Point out each Plasmodium parasite.
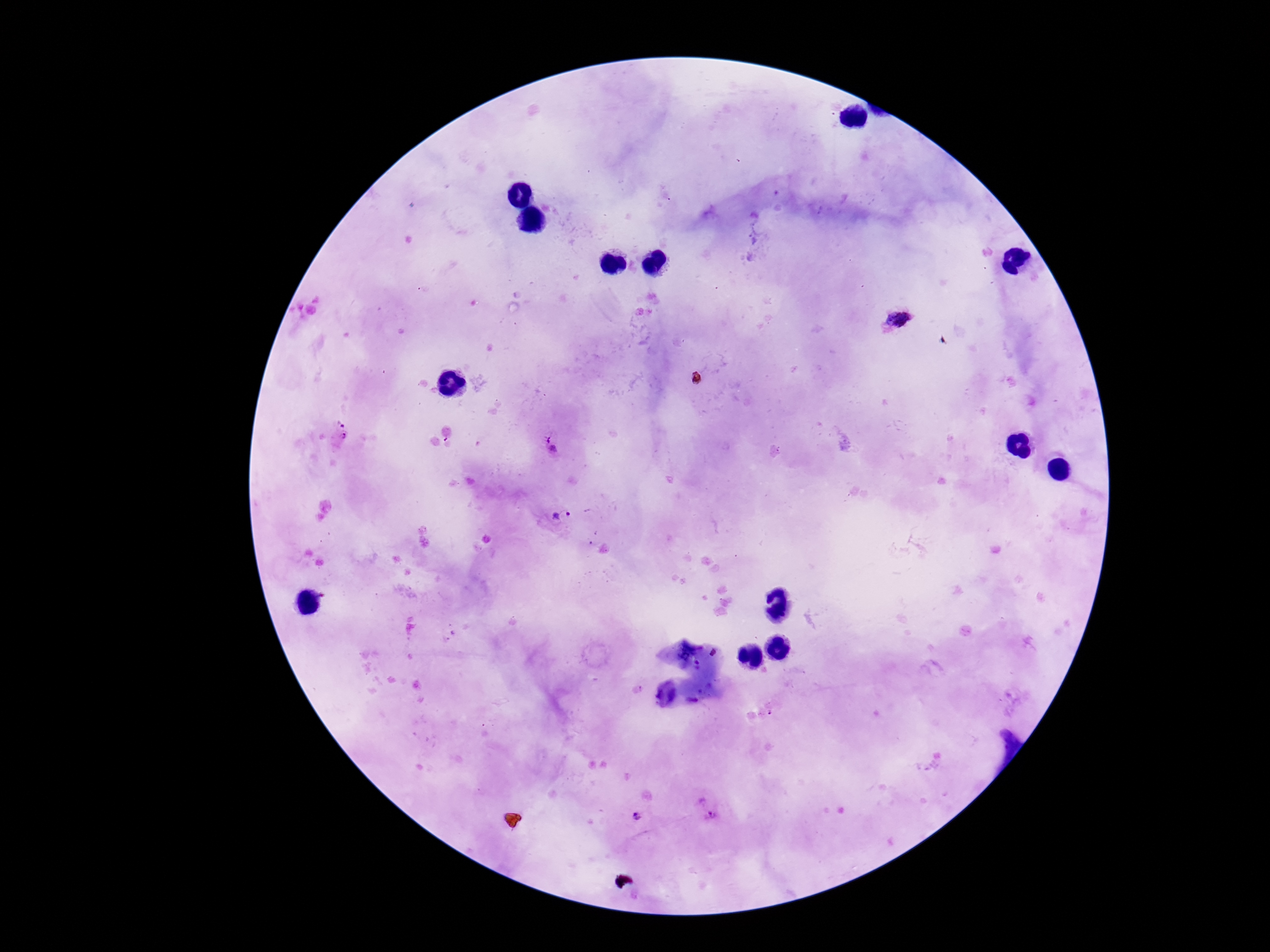
Approximate centers as [x, y] in pixels.
Plasmodium parasites: [897, 320], [339, 421], [342, 441], [553, 446], [561, 516], [706, 808], [635, 817].

Photographed through the microscope eyepiece with a smartphone camera. Giemsa stain. Patient malaria status: infected. Thick blood film. Image is 1270×952 pixels. 100x magnification. One field from this slide.